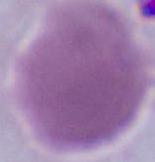
identification: red blood cell
modality: micrograph
magnification: 1000x